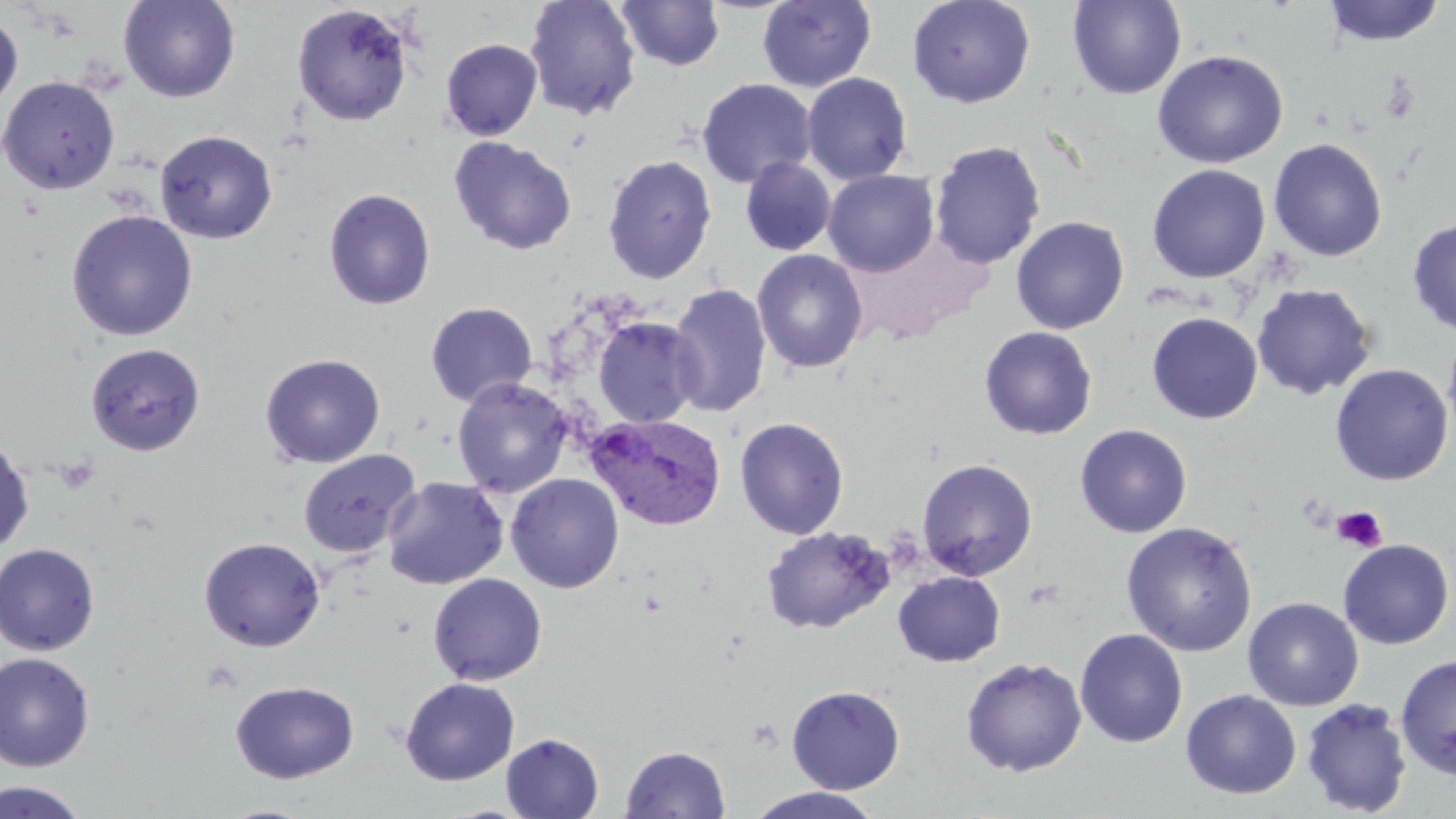 Approximate bounding boxes as (x1, y1, x2, y2) in pixels. Uninfected red blood cell locations: (119, 0, 240, 103), (524, 0, 641, 121), (757, 0, 876, 92), (907, 0, 1036, 108), (1067, 0, 1186, 99), (1323, 0, 1445, 46), (617, 1, 726, 71), (292, 4, 413, 126), (0, 11, 23, 116), (441, 38, 543, 141), (1152, 49, 1289, 169), (802, 72, 913, 185), (1, 76, 120, 195), (697, 78, 816, 189), (155, 130, 277, 244), (448, 136, 577, 255), (1268, 138, 1387, 262), (928, 140, 1046, 270), (603, 154, 716, 283), (740, 157, 837, 255), (1147, 164, 1270, 283), (823, 170, 939, 276), (323, 188, 436, 310), (65, 210, 198, 342), (1011, 216, 1128, 334), (1407, 218, 1456, 336), (752, 249, 869, 374), (1251, 283, 1376, 400), (668, 284, 771, 417), (425, 302, 538, 407), (1147, 312, 1263, 424), (593, 316, 703, 428), (979, 326, 1097, 440), (1442, 326, 1456, 445), (85, 343, 206, 455), (260, 353, 386, 468), (1330, 364, 1453, 485), (452, 377, 574, 498), (734, 417, 849, 539), (1075, 424, 1192, 538), (0, 439, 34, 553), (298, 450, 420, 559), (917, 458, 1038, 581), (506, 473, 624, 593), (382, 477, 508, 589), (1121, 521, 1257, 656), (761, 526, 894, 635), (198, 536, 325, 651), (1338, 539, 1454, 649), (0, 542, 100, 656), (893, 572, 1005, 666), (429, 573, 547, 686), (1243, 597, 1363, 711), (1075, 628, 1188, 747), (0, 651, 95, 771), (1395, 654, 1456, 780), (961, 657, 1087, 776), (400, 677, 519, 785), (230, 681, 359, 783), (786, 684, 905, 794), (1181, 689, 1302, 799), (1300, 698, 1412, 817), (501, 733, 604, 818), (621, 745, 730, 819), (0, 780, 90, 818), (747, 786, 884, 819), (216, 803, 321, 818). Plasmodium vivax-infected red blood cell locations: (586, 413, 727, 530). Platelet locations: (1380, 73, 1420, 124), (56, 457, 100, 495), (1332, 506, 1387, 552). Slide-level diagnosis: Plasmodium vivax. Single field of view. Optical microscopy. Image is 1456×819 pixels. Thin blood smear. May-Grünwald-Giemsa-stained preparation. Captured at 1000x magnification.